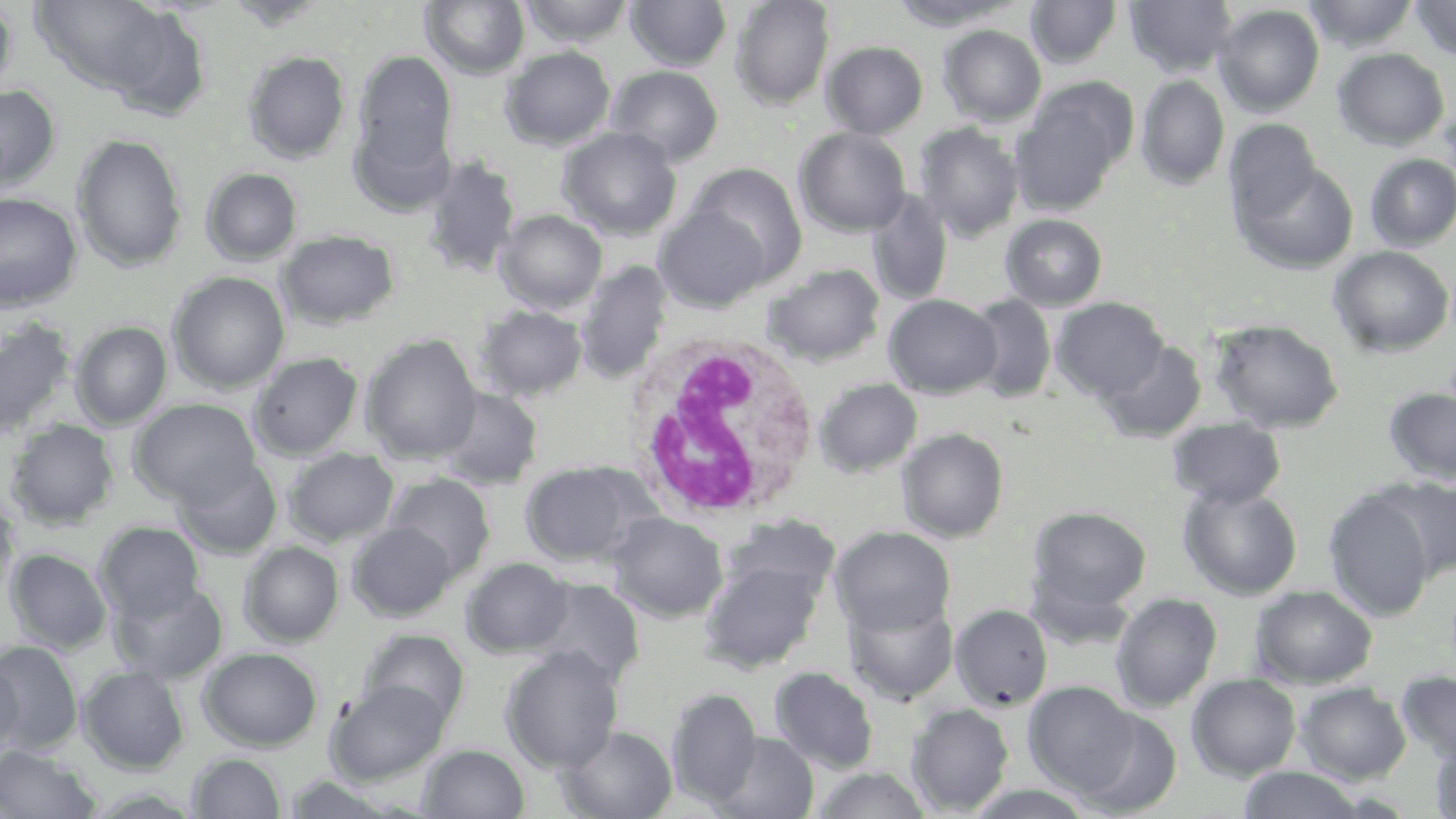

Summary:
  - Coordinate format: approximate bounding boxes as (x1,y1)-(x2,y2) corner pairs in pixels
  - White blood cell locations: (623,332)-(821,526)
  - Uninfected red blood cell locations: (0,0)-(17,99), (25,0)-(170,98), (225,0)-(328,30), (519,0)-(636,47), (730,0)-(835,110), (888,0)-(1020,30), (1125,0)-(1238,77), (1303,0)-(1419,51), (1410,0)-(1456,62), (421,1)-(530,79), (625,1)-(732,71), (1026,1)-(1122,69), (1214,4)-(1325,116), (121,11)-(212,116), (938,24)-(1047,127), (822,41)-(928,138), (501,46)-(616,150), (1332,48)-(1450,150), (1353,48)-(1454,252), (353,50)-(458,175), (242,51)-(351,164), (606,65)-(724,167), (1136,74)-(1230,191), (1010,82)-(1134,217), (0,84)-(61,192), (1224,119)-(1322,230), (913,122)-(1024,242), (558,127)-(683,240), (794,127)-(911,236), (72,134)-(186,272), (1365,153)-(1456,251), (420,155)-(520,279), (1237,161)-(1358,274), (685,162)-(808,283), (201,167)-(303,265), (866,190)-(953,306), (0,192)-(83,311), (654,205)-(773,312), (495,209)-(608,313), (1001,214)-(1108,310), (277,230)-(400,329), (1329,246)-(1454,357), (575,261)-(674,383), (764,263)-(886,366), (168,271)-(290,393), (884,294)-(1001,399), (966,294)-(1058,402), (1052,297)-(1169,401), (474,305)-(589,401), (0,318)-(77,442), (1209,319)-(1344,434), (70,321)-(172,429), (360,333)-(483,463), (1098,340)-(1207,442), (248,352)-(364,460), (814,378)-(922,477), (434,387)-(544,490), (1384,387)-(1456,484), (129,398)-(261,506), (1168,417)-(1286,508), (5,419)-(119,529), (896,428)-(1008,542), (283,447)-(400,547), (174,456)-(282,559), (519,461)-(653,568), (385,473)-(495,581), (1379,475)-(1456,581), (1178,483)-(1303,600), (1323,489)-(1436,621), (0,492)-(21,600), (1028,506)-(1151,617), (608,512)-(728,622), (721,514)-(841,603), (94,521)-(205,623), (347,522)-(457,621), (831,526)-(956,636), (239,541)-(344,647), (6,548)-(112,654), (462,557)-(572,657), (699,559)-(823,674), (531,577)-(645,686), (112,581)-(228,684), (1249,584)-(1377,689), (1110,592)-(1223,712), (843,594)-(959,704), (950,604)-(1053,711), (358,628)-(470,728), (0,640)-(83,755), (501,645)-(624,773), (198,647)-(323,751), (0,653)-(24,758), (78,666)-(189,773), (769,666)-(879,773), (1396,671)-(1456,766), (1186,673)-(1302,780), (327,680)-(450,784), (1023,680)-(1141,798), (1295,682)-(1412,783), (668,688)-(762,807), (906,704)-(1014,815), (1072,706)-(1183,816), (558,725)-(678,819), (711,732)-(819,819), (1428,735)-(1456,819), (0,744)-(100,818), (419,744)-(529,818), (187,752)-(287,819), (812,767)-(932,818), (1237,767)-(1366,819), (962,784)-(1098,819)
  - Slide-level diagnosis: no evidence of blood parasites
  - Stain: May-Grünwald-Giemsa
  - Magnification: 1000x
  - Modality: optical microscopy
  - Image size: 1456×819 pixels
  - Field of view: one of a larger specimen
  - Preparation: thin blood smear